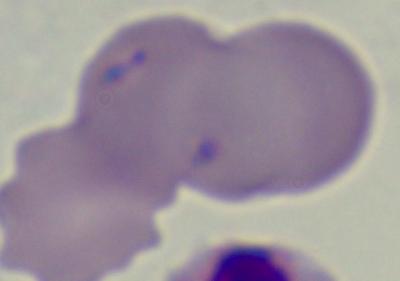
A Babesia parasite is shown. Micrograph. 1000x magnification.